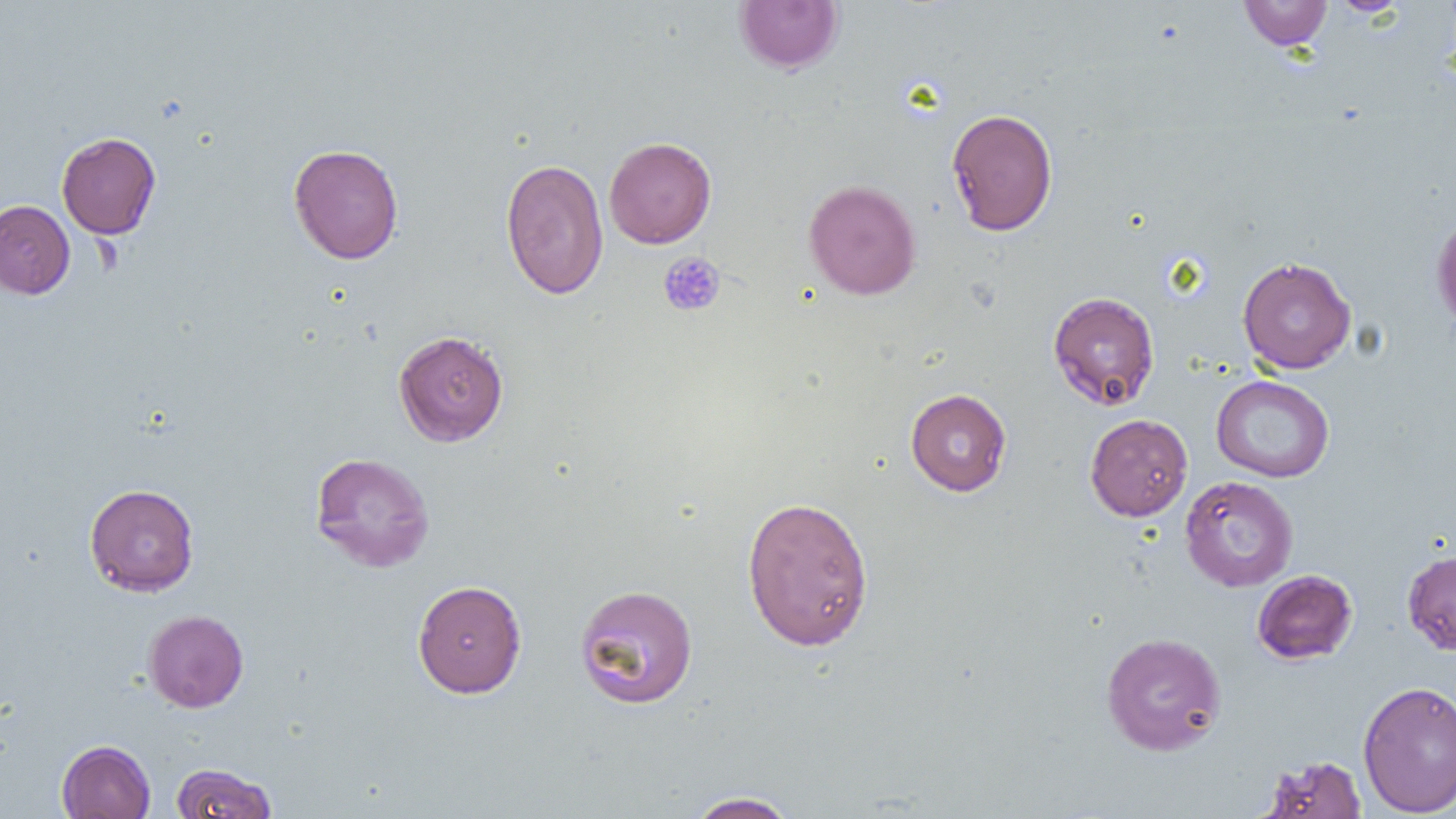
Summary:
  - Coordinate format: approximate bounding boxes as [x1, y1, x2, y2] in pixels
  - Uninfected red blood cell locations: [734, 0, 844, 73], [1239, 0, 1332, 50], [1327, 0, 1410, 17], [946, 107, 1058, 236], [57, 132, 161, 239], [604, 136, 716, 249], [288, 143, 403, 264], [500, 157, 609, 300], [804, 179, 921, 300], [0, 200, 75, 299], [1431, 212, 1456, 331], [1237, 256, 1356, 374], [1047, 291, 1160, 410], [393, 330, 509, 446], [1211, 375, 1334, 483], [905, 388, 1012, 496], [1085, 413, 1193, 521], [310, 451, 435, 572], [1179, 475, 1299, 592], [84, 483, 199, 596], [741, 495, 875, 651], [1402, 550, 1456, 655], [1252, 569, 1357, 665], [412, 580, 527, 697], [575, 583, 698, 709], [142, 609, 249, 712], [1101, 631, 1227, 756], [1357, 679, 1456, 817], [56, 739, 155, 819], [1260, 754, 1367, 818], [169, 762, 278, 818], [686, 791, 801, 818]
  - Platelet locations: [658, 251, 726, 317]
  - Slide-level diagnosis: negative for blood parasites
  - Magnification: 1000x
  - Image size: 1456×819 pixels
  - Preparation: thin blood film
  - Field of view: one of a larger specimen
  - Modality: optical microscopy